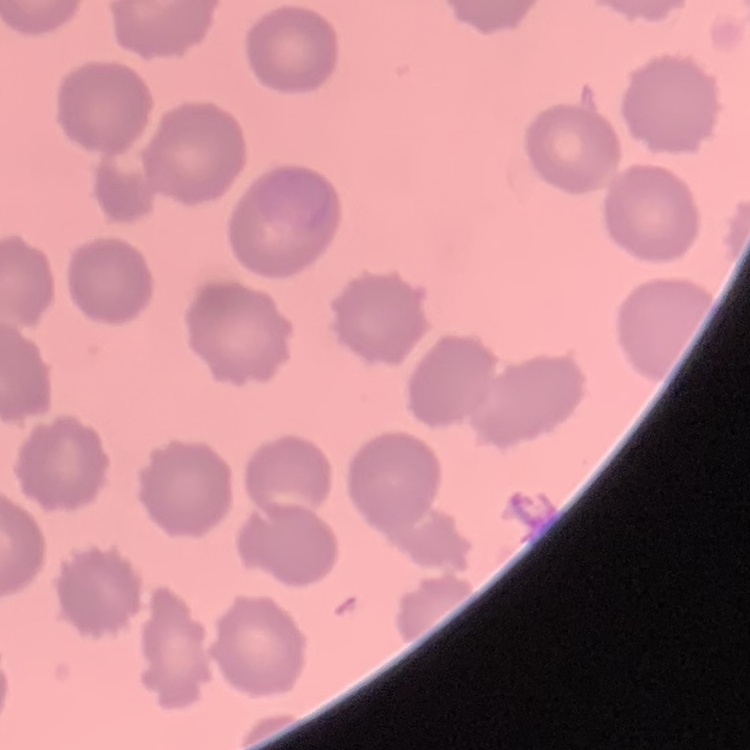

The red blood cells show no rouleaux formation. Field's or Giemsa stain. One tile cut from a larger photomicrograph. Thin blood film.